State the blood parasite species.
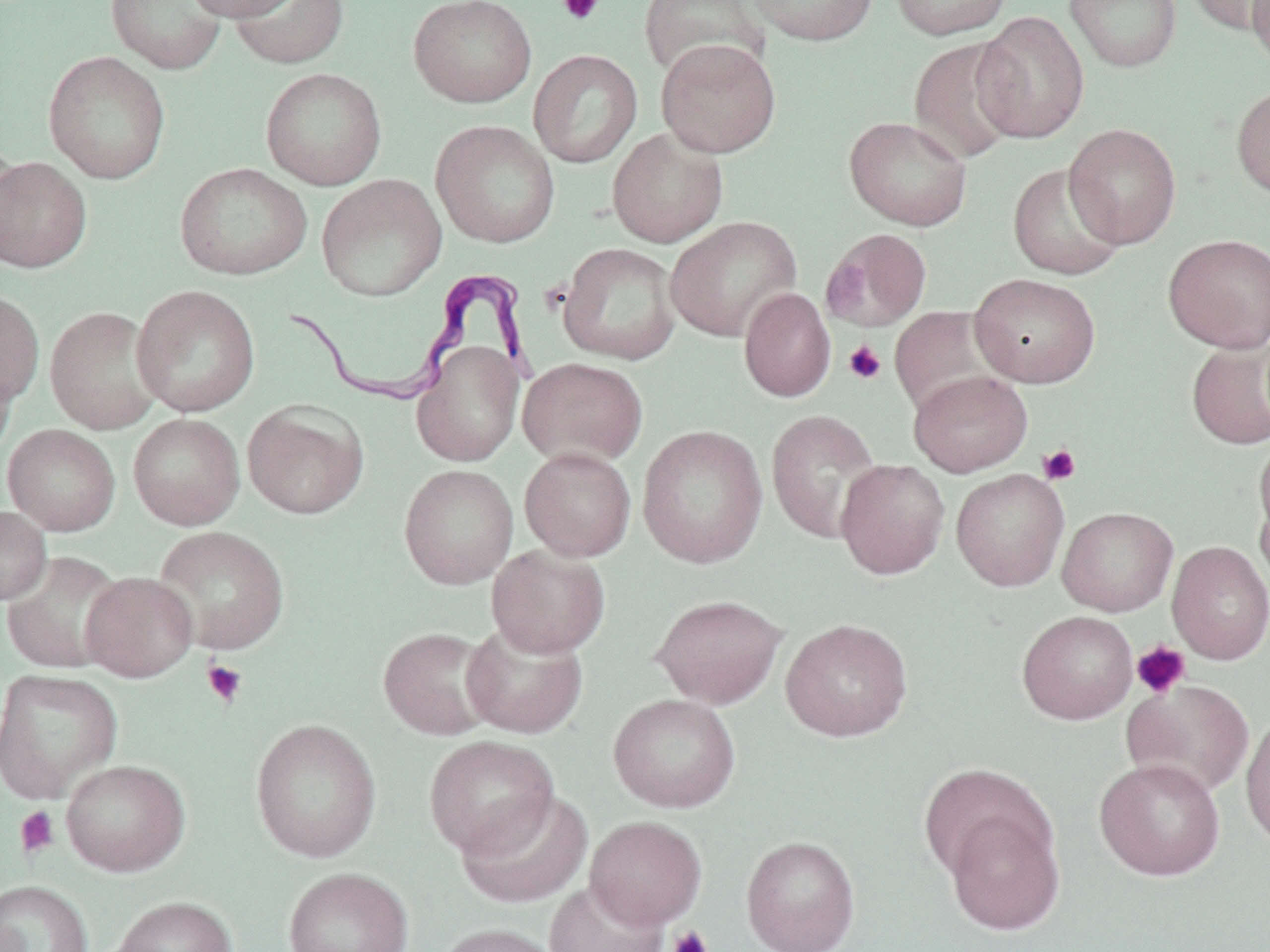
Trypanosoma brucei.

{
  "magnification": "1000x",
  "trypanosoma_brucei_locations": "approximate bounding boxes as [x1, y1, x2, y2] in pixels: [274, 267, 539, 406]",
  "preparation": "thin blood film",
  "field_of_view": "single",
  "uninfected_red_blood_cell_locations_subset": "approximate bounding boxes as [x1, y1, x2, y2] in pixels: [105, 0, 228, 75], [183, 0, 302, 21], [230, 0, 349, 69], [408, 0, 537, 108], [745, 0, 879, 46], [888, 0, 1012, 40], [1064, 0, 1182, 73], [1184, 0, 1269, 36], [1248, 0, 1269, 71], [639, 1, 770, 82], [972, 11, 1090, 143], [907, 36, 1025, 165], [655, 38, 781, 158], [528, 49, 643, 169], [43, 50, 171, 184], [260, 67, 387, 190], [1231, 83, 1270, 200], [843, 115, 973, 231], [430, 120, 560, 248], [1063, 123, 1182, 249], [607, 127, 728, 248], [0, 138, 22, 263], [0, 156, 92, 273], [1007, 162, 1126, 280], [174, 163, 312, 281], [316, 174, 447, 302], [665, 216, 802, 342], [820, 228, 933, 332], [1163, 234, 1270, 353], [558, 243, 681, 365], [969, 273, 1101, 388], [131, 284, 261, 417], [738, 287, 836, 402], [0, 289, 45, 408], [44, 306, 164, 434], [1186, 338, 1270, 450], [411, 341, 523, 467], [0, 352, 17, 463], [517, 357, 648, 468], [908, 370, 1033, 477], [243, 401, 368, 520], [765, 409, 883, 544], [128, 413, 245, 530], [2, 424, 120, 536], [637, 425, 768, 569], [1254, 436, 1270, 544], [519, 447, 636, 561], [835, 459, 950, 579], [398, 464, 519, 589], [951, 469, 1070, 591], [1255, 487, 1270, 599], [0, 505, 51, 605], [1057, 506, 1178, 616], [153, 526, 290, 655], [1167, 541, 1270, 664], [486, 544, 611, 658], [2, 551, 127, 673], [80, 571, 199, 681], [649, 594, 788, 709], [780, 618, 913, 742], [461, 619, 588, 740], [378, 626, 499, 740], [0, 668, 122, 801], [1122, 679, 1254, 798], [608, 693, 740, 813], [1240, 710, 1270, 853], [249, 717, 382, 863], [424, 735, 558, 857], [1094, 757, 1225, 881], [60, 759, 191, 876], [918, 761, 1051, 881], [456, 790, 593, 909], [943, 806, 1065, 936], [584, 815, 707, 930], [741, 835, 860, 951], [282, 866, 413, 952], [0, 880, 93, 952], [543, 880, 667, 952], [111, 895, 237, 952], [434, 922, 563, 952]",
  "image_size": "1270×952 pixels",
  "stain": "May-Grünwald-Giemsa",
  "modality": "light microscopy",
  "platelet_locations_subset": "approximate bounding boxes as [x1, y1, x2, y2] in pixels: [557, 0, 604, 25], [821, 259, 869, 318], [843, 340, 887, 385], [1038, 444, 1079, 486], [1130, 640, 1191, 699], [201, 659, 248, 708], [14, 806, 60, 858], [666, 926, 714, 952]"
}